State the blood parasite species.
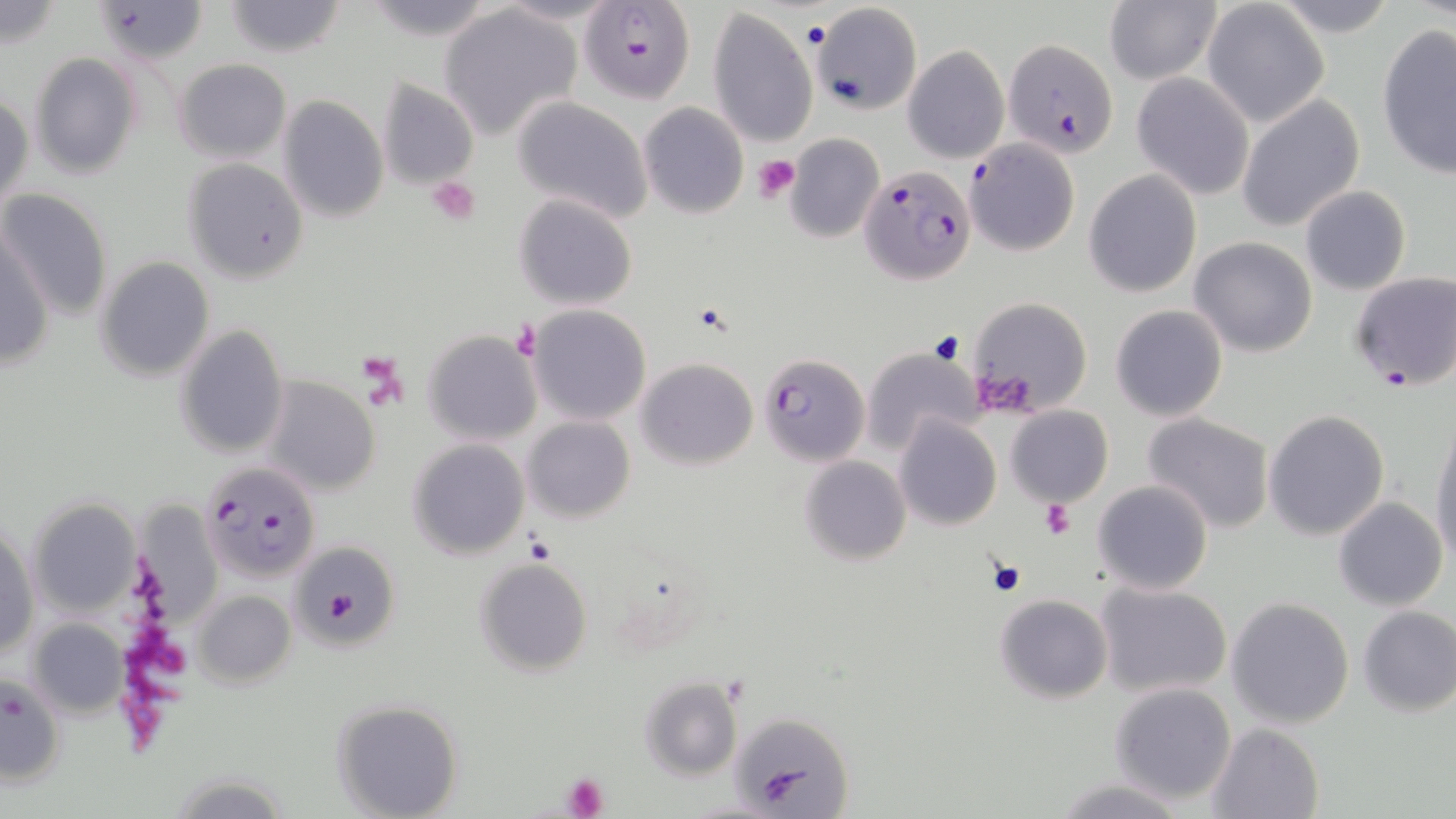

Plasmodium falciparum.

Summary:
  - Coordinate format: approximate bounding boxes as (x1, y1, x2, y2) in pixels
  - Plasmodium falciparum-infected red blood cell locations: (580, 2, 693, 104), (94, 3, 208, 63), (1003, 37, 1118, 157), (965, 138, 1080, 257), (861, 164, 977, 284), (1347, 270, 1456, 391), (759, 353, 870, 464), (201, 460, 323, 581)
  - Uninfected red blood cell locations: (0, 1, 63, 49), (222, 1, 346, 56), (808, 1, 924, 115), (1102, 1, 1220, 86), (1201, 2, 1330, 128), (439, 4, 584, 140), (706, 6, 818, 148), (1377, 25, 1456, 180), (903, 45, 1008, 163), (29, 53, 143, 179), (173, 57, 292, 163), (1131, 72, 1255, 200), (376, 79, 479, 191), (0, 92, 32, 216), (277, 95, 389, 222), (1236, 96, 1366, 232), (512, 98, 653, 223), (639, 103, 749, 219), (785, 135, 884, 243), (182, 159, 309, 284), (1084, 170, 1201, 296), (1299, 185, 1412, 295), (1, 187, 113, 322), (513, 194, 638, 311), (1, 224, 51, 377), (1189, 236, 1318, 357), (96, 257, 214, 380), (965, 297, 1093, 417), (1110, 303, 1228, 422), (528, 305, 651, 424), (175, 325, 288, 458), (423, 331, 541, 445), (863, 348, 979, 453), (636, 357, 758, 470), (262, 377, 380, 495), (1006, 403, 1112, 507), (1263, 409, 1390, 541), (1142, 412, 1276, 533), (1429, 412, 1456, 568), (522, 415, 635, 522), (896, 415, 1001, 531), (407, 439, 529, 559), (799, 456, 912, 566), (1092, 479, 1214, 595), (1333, 497, 1449, 609), (28, 499, 142, 619), (131, 500, 222, 629), (1, 525, 39, 665), (297, 546, 397, 646), (474, 557, 594, 675), (1093, 580, 1234, 699), (191, 589, 296, 688), (994, 594, 1112, 704), (1226, 597, 1354, 729), (1356, 606, 1456, 718), (27, 618, 128, 718), (1, 672, 65, 786), (639, 677, 741, 780), (1109, 681, 1237, 804), (329, 699, 463, 818), (730, 709, 854, 814), (1207, 722, 1325, 818), (1052, 777, 1189, 818)
  - Platelet locations: (800, 18, 830, 51), (752, 155, 802, 202), (426, 178, 479, 226), (930, 333, 967, 365), (1040, 499, 1075, 540), (524, 532, 555, 564), (987, 558, 1027, 596), (327, 591, 360, 619), (563, 773, 610, 818)
  - Magnification: 1000x
  - Stain: May-Grünwald-Giemsa
  - Modality: light microscopy
  - Image size: 1456×819 pixels
  - Field of view: single
  - Preparation: thin blood smear